Locate leukocytes (white blood cells).
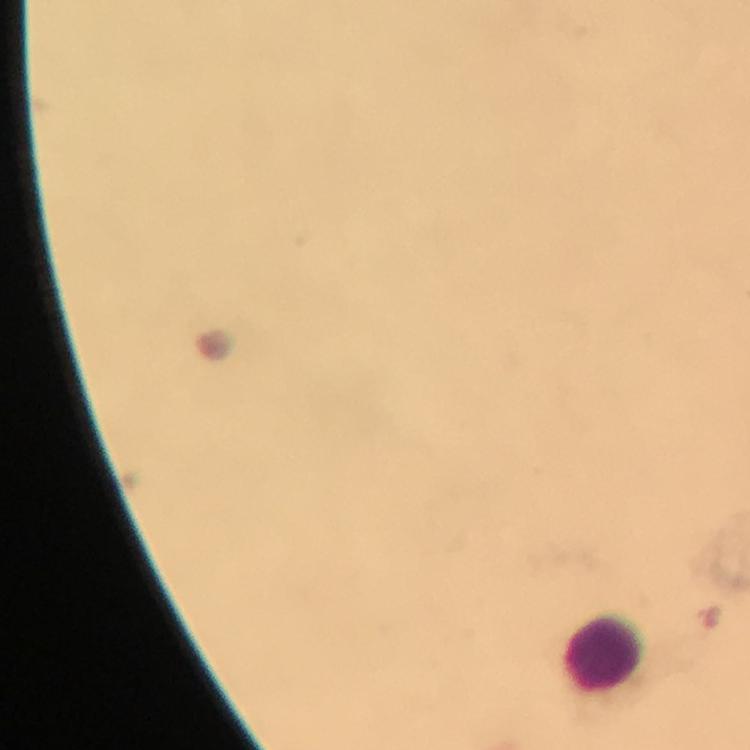

Approximate centers as (x, y) in pixels.
Leukocytes: (604, 647).

cropped from = one field of view
magnification = 100x
context = from a malaria diagnostic workup
image size = 750×750 pixels
capture = smartphone camera through the microscope
immersion oil = used
Plasmodium parasites = none seen
preparation = thick blood smear
stain = Giemsa